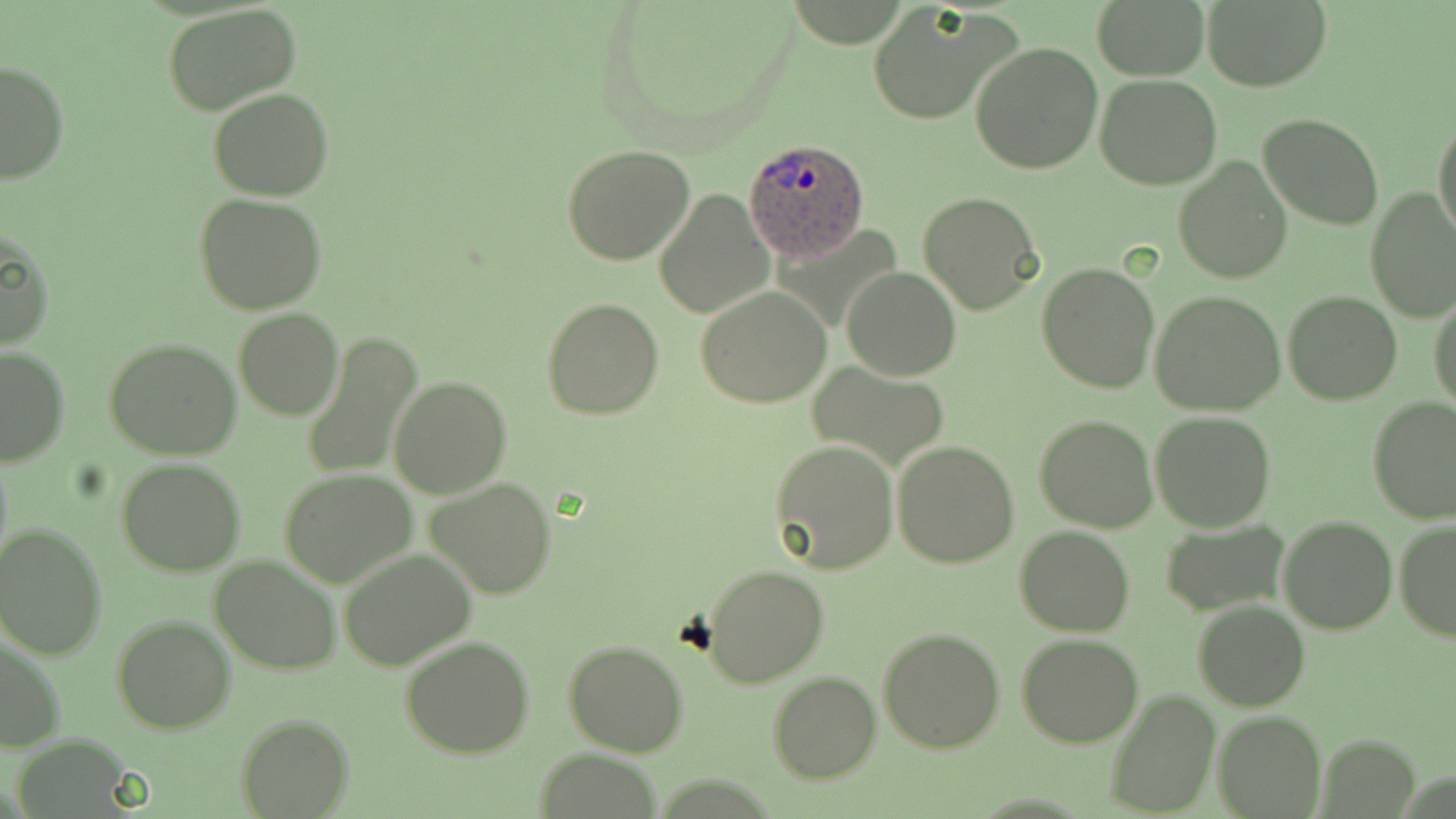

Approximate bounding boxes as [x1, y1, x2, y2] in pixels. Uninfected red blood cell locations: [1091, 0, 1212, 81], [1202, 0, 1331, 91], [866, 2, 1019, 126], [163, 4, 301, 116], [971, 40, 1103, 174], [0, 60, 71, 187], [1095, 73, 1223, 189], [209, 88, 333, 201], [1259, 112, 1383, 228], [1432, 115, 1456, 243], [564, 143, 694, 264], [1172, 155, 1293, 285], [1365, 186, 1456, 323], [655, 189, 774, 319], [917, 192, 1043, 316], [196, 194, 326, 314], [0, 228, 55, 353], [1037, 263, 1160, 393], [843, 267, 961, 380], [695, 286, 833, 408], [1149, 290, 1286, 415], [1283, 290, 1402, 405], [1429, 292, 1455, 415], [542, 298, 665, 420], [234, 309, 343, 421], [264, 312, 390, 450], [300, 331, 422, 481], [103, 338, 243, 459], [0, 344, 71, 465], [812, 363, 949, 471], [389, 375, 511, 497], [1367, 397, 1456, 523], [1150, 411, 1275, 531], [1034, 415, 1158, 532], [767, 440, 898, 576], [893, 442, 1020, 569], [115, 456, 247, 576], [279, 469, 416, 586], [427, 477, 558, 598], [1279, 515, 1398, 634], [1160, 519, 1290, 616], [1394, 521, 1456, 642], [0, 525, 106, 659], [1014, 526, 1136, 637], [338, 546, 479, 669], [210, 554, 341, 675], [699, 565, 829, 687], [1193, 599, 1309, 712], [111, 615, 235, 733], [877, 627, 1004, 752], [1017, 633, 1145, 748], [1, 634, 67, 751], [400, 635, 534, 758], [564, 638, 689, 756], [767, 672, 882, 784], [1102, 691, 1221, 817], [1213, 709, 1326, 819], [235, 715, 354, 818], [1317, 734, 1421, 817], [533, 749, 662, 819]. Plasmodium ovale-infected red blood cell locations: [746, 139, 870, 261]. Slide-level diagnosis: Plasmodium ovale. Image is 1456×819 pixels. Light microscopy. One field of a larger specimen. Thin blood smear. May-Grünwald-Giemsa-stained preparation. Captured at 1000x magnification.